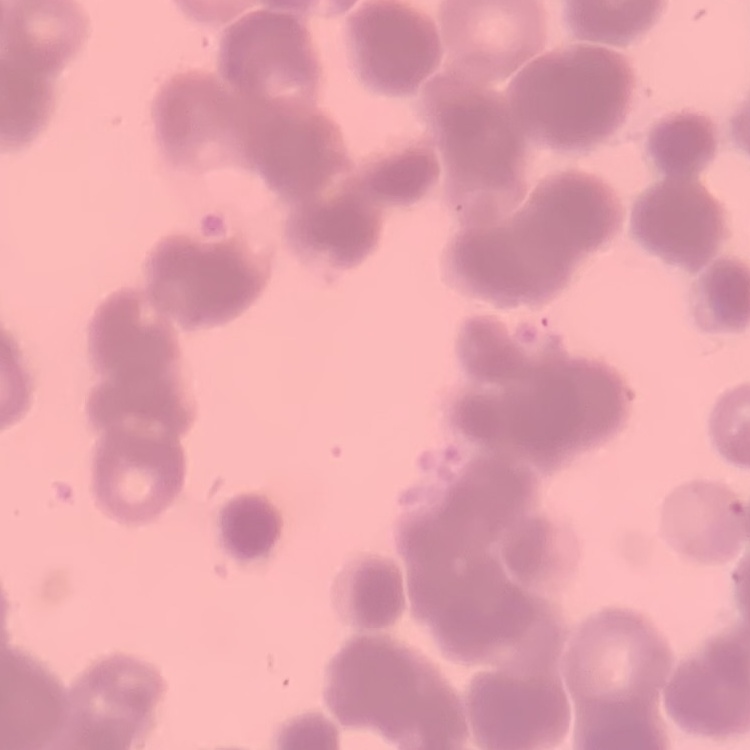
red_blood_cell_morphology: rouleaux formation
image_type: one tile cut from a larger photomicrograph
preparation: thin peripheral smear
stain: Field's or Giemsa